Locate every blood parasite and identify its species.
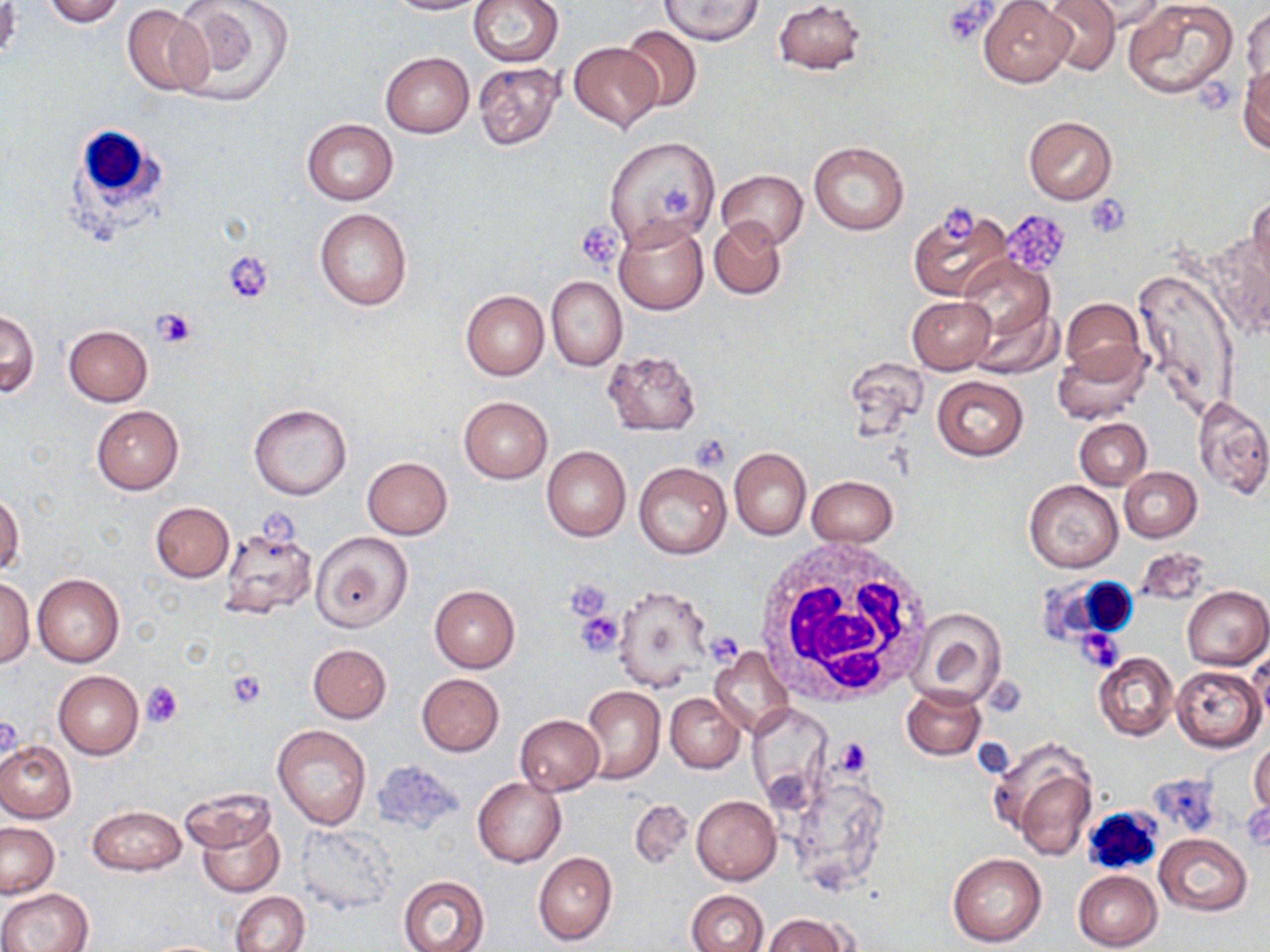

No blood parasites seen.

Approximate bounding boxes as named x1/y1/x2/y2 corners in pixels. Platelet locations: (x1=943, y1=1, x2=993, y2=45), (x1=1197, y1=76, x2=1235, y2=120), (x1=659, y1=184, x2=693, y2=215), (x1=1085, y1=196, x2=1129, y2=237), (x1=942, y1=204, x2=978, y2=239), (x1=1000, y1=209, x2=1072, y2=275), (x1=577, y1=220, x2=623, y2=269), (x1=223, y1=253, x2=274, y2=303), (x1=152, y1=306, x2=200, y2=348), (x1=690, y1=435, x2=733, y2=471), (x1=564, y1=579, x2=612, y2=622), (x1=574, y1=610, x2=625, y2=656), (x1=1078, y1=628, x2=1123, y2=670), (x1=709, y1=632, x2=745, y2=666), (x1=225, y1=670, x2=267, y2=710), (x1=141, y1=680, x2=183, y2=728), (x1=1, y1=716, x2=22, y2=761). White blood cell locations: (x1=66, y1=119, x2=168, y2=233), (x1=756, y1=540, x2=933, y2=705), (x1=1045, y1=577, x2=1140, y2=643), (x1=1080, y1=804, x2=1163, y2=876). Uninfected red blood cell locations: (x1=40, y1=0, x2=125, y2=27), (x1=171, y1=0, x2=291, y2=106), (x1=387, y1=0, x2=488, y2=15), (x1=468, y1=0, x2=563, y2=67), (x1=657, y1=0, x2=766, y2=45), (x1=774, y1=0, x2=867, y2=74), (x1=979, y1=0, x2=1075, y2=87), (x1=1039, y1=0, x2=1119, y2=75), (x1=1076, y1=0, x2=1166, y2=33), (x1=1124, y1=1, x2=1239, y2=102), (x1=0, y1=3, x2=21, y2=65), (x1=123, y1=4, x2=210, y2=96), (x1=1243, y1=4, x2=1269, y2=92), (x1=618, y1=26, x2=703, y2=112), (x1=569, y1=42, x2=662, y2=131), (x1=380, y1=52, x2=474, y2=137), (x1=473, y1=60, x2=564, y2=152), (x1=1239, y1=64, x2=1269, y2=152), (x1=1024, y1=116, x2=1117, y2=205), (x1=302, y1=119, x2=397, y2=205), (x1=603, y1=135, x2=720, y2=250), (x1=809, y1=141, x2=909, y2=234), (x1=714, y1=169, x2=807, y2=250), (x1=1247, y1=195, x2=1270, y2=290), (x1=907, y1=203, x2=1015, y2=303), (x1=314, y1=208, x2=413, y2=311), (x1=709, y1=217, x2=787, y2=298), (x1=614, y1=218, x2=708, y2=315), (x1=959, y1=256, x2=1054, y2=346), (x1=1135, y1=268, x2=1240, y2=420), (x1=545, y1=275, x2=626, y2=371), (x1=462, y1=291, x2=547, y2=379), (x1=908, y1=296, x2=995, y2=373), (x1=1059, y1=298, x2=1147, y2=385), (x1=967, y1=299, x2=1060, y2=379), (x1=0, y1=311, x2=40, y2=396), (x1=64, y1=325, x2=153, y2=406), (x1=1052, y1=345, x2=1150, y2=424), (x1=602, y1=349, x2=703, y2=437), (x1=931, y1=375, x2=1028, y2=461), (x1=458, y1=396, x2=552, y2=483), (x1=1193, y1=396, x2=1270, y2=499), (x1=248, y1=403, x2=353, y2=501), (x1=91, y1=405, x2=184, y2=494), (x1=1074, y1=418, x2=1151, y2=490), (x1=542, y1=445, x2=631, y2=541), (x1=729, y1=448, x2=811, y2=541), (x1=362, y1=456, x2=452, y2=539), (x1=634, y1=462, x2=731, y2=559), (x1=1120, y1=467, x2=1203, y2=542), (x1=806, y1=476, x2=898, y2=548), (x1=1025, y1=481, x2=1123, y2=572), (x1=1, y1=493, x2=25, y2=577), (x1=150, y1=502, x2=234, y2=581), (x1=217, y1=525, x2=319, y2=619), (x1=311, y1=531, x2=413, y2=632), (x1=1134, y1=549, x2=1213, y2=606), (x1=33, y1=573, x2=124, y2=666), (x1=0, y1=576, x2=36, y2=668), (x1=612, y1=584, x2=713, y2=692), (x1=429, y1=586, x2=521, y2=672), (x1=1182, y1=586, x2=1269, y2=670), (x1=909, y1=607, x2=1008, y2=707), (x1=308, y1=643, x2=391, y2=723), (x1=1248, y1=645, x2=1269, y2=730), (x1=709, y1=647, x2=794, y2=737), (x1=1094, y1=652, x2=1178, y2=740), (x1=1172, y1=665, x2=1264, y2=752), (x1=53, y1=671, x2=143, y2=758), (x1=417, y1=673, x2=504, y2=756), (x1=582, y1=685, x2=664, y2=783), (x1=901, y1=687, x2=987, y2=760), (x1=665, y1=692, x2=744, y2=773), (x1=515, y1=715, x2=604, y2=795), (x1=273, y1=724, x2=372, y2=830), (x1=992, y1=738, x2=1099, y2=858), (x1=1249, y1=740, x2=1270, y2=816), (x1=0, y1=742, x2=75, y2=823), (x1=372, y1=757, x2=465, y2=836), (x1=782, y1=760, x2=891, y2=900), (x1=473, y1=777, x2=565, y2=867), (x1=181, y1=786, x2=276, y2=852), (x1=691, y1=794, x2=780, y2=885), (x1=629, y1=799, x2=693, y2=869), (x1=88, y1=805, x2=185, y2=875), (x1=196, y1=814, x2=285, y2=898), (x1=0, y1=823, x2=59, y2=898), (x1=295, y1=823, x2=397, y2=914), (x1=1155, y1=835, x2=1252, y2=916), (x1=534, y1=852, x2=616, y2=945), (x1=946, y1=852, x2=1046, y2=947), (x1=1072, y1=870, x2=1163, y2=951), (x1=398, y1=875, x2=490, y2=952), (x1=1, y1=888, x2=93, y2=952), (x1=686, y1=890, x2=769, y2=952), (x1=231, y1=891, x2=310, y2=952), (x1=763, y1=913, x2=853, y2=951). Slide-level diagnosis: negative for blood parasites. 1000x magnification. One field of a larger specimen. Image is 1270×952 pixels. May-Grünwald-Giemsa stain. Light microscopy. Thin blood smear.